Point out each Plasmodium parasite and each leukocyte.
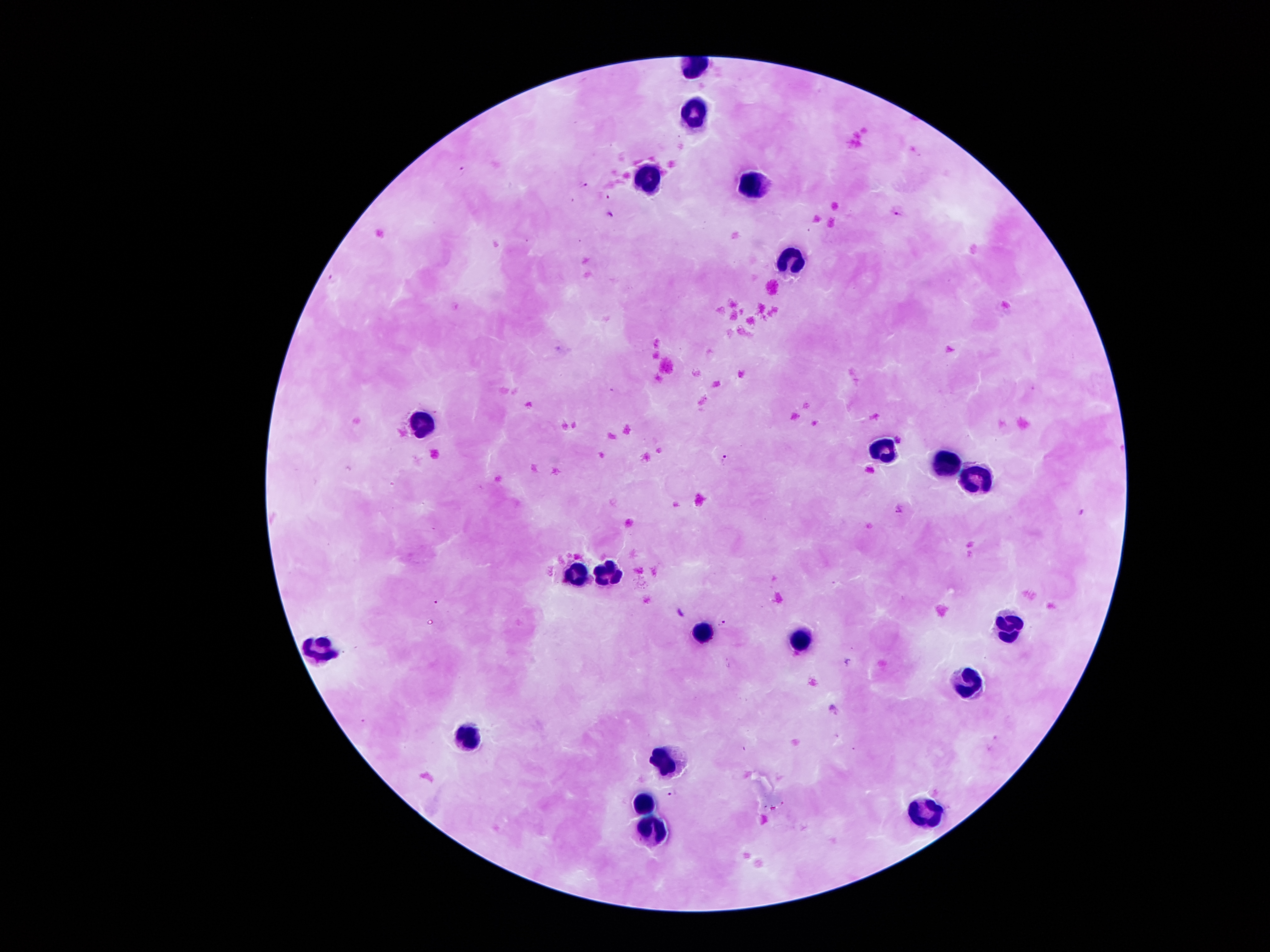

Approximate centers as (x, y) in pixels.
Plasmodium parasites: (463, 168), (584, 184), (607, 198), (897, 213), (611, 216), (330, 278), (725, 457), (899, 510), (1082, 511), (723, 624), (672, 794).
Leukocytes: (694, 115), (649, 177), (749, 181), (790, 261), (420, 420), (883, 451), (943, 464), (977, 481), (576, 572), (609, 573), (1009, 622), (698, 630), (797, 636), (318, 643), (973, 684), (470, 733), (664, 758), (644, 799), (923, 813), (652, 829).

Summary:
  - Image size: 1270×952 pixels
  - Stain: Giemsa
  - Preparation: thick peripheral-blood smear
  - Magnification: 100x
  - Capture: smartphone through the microscope eyepiece
  - Field of view: single
  - Patient malaria status: positive for Plasmodium falciparum